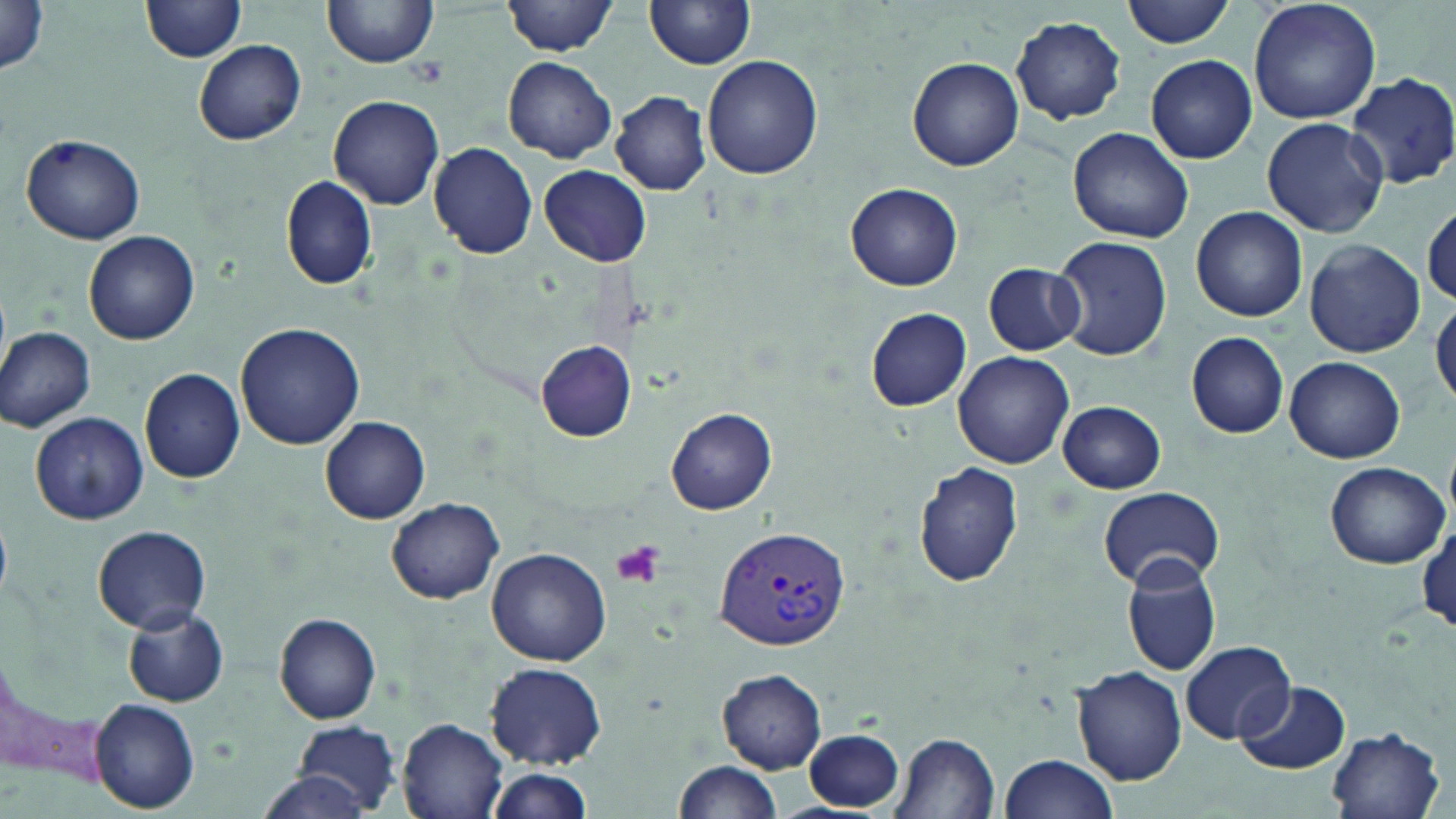
slide_level_diagnosis: Plasmodium vivax
image_size: 1456×819 pixels
platelet_locations: 'approximate bounding boxes as (x1,y1)-(x2,y2) corner pairs in pixels: (412,57)-(448,87), (612,540)-(667,589)'
plasmodium_vivax_infected_red_blood_cell_locations: 'approximate bounding boxes as (x1,y1)-(x2,y2) corner pairs in pixels: (714,524)-(853,649)'
field_of_view: one of a larger specimen
magnification: 1000x
modality: optical microscopy
uninfected_red_blood_cell_locations: 'approximate bounding boxes as (x1,y1)-(x2,y2) corner pairs in pixels: (323,0)-(437,69), (502,0)-(618,56), (646,0)-(755,70), (1122,0)-(1237,47), (1248,0)-(1382,124), (140,2)-(246,64), (0,4)-(52,77), (1011,16)-(1127,124), (193,38)-(306,146), (700,54)-(824,180), (503,55)-(617,163), (1144,55)-(1258,164), (907,57)-(1024,171), (1347,71)-(1456,190), (611,91)-(712,195), (328,95)-(445,210), (1261,118)-(1389,238), (1067,127)-(1193,244), (20,132)-(146,244), (428,143)-(537,259), (538,165)-(651,266), (280,176)-(379,290), (846,182)-(964,291), (1421,197)-(1456,308), (1191,207)-(1307,322), (82,230)-(200,346), (1052,236)-(1172,361), (1303,239)-(1426,357), (983,261)-(1085,355), (1430,295)-(1456,413), (865,307)-(972,412), (235,321)-(366,450), (0,326)-(97,432), (1187,331)-(1290,439), (535,340)-(637,441), (952,351)-(1074,469), (1283,355)-(1405,463), (139,367)-(245,484), (1057,401)-(1166,492), (666,406)-(776,514), (30,411)-(148,525), (321,416)-(430,523), (1324,461)-(1450,569), (913,462)-(1024,588), (1097,486)-(1226,589), (386,497)-(505,603), (1413,518)-(1456,635), (92,525)-(210,634), (486,547)-(611,666), (1121,557)-(1225,678), (122,606)-(228,706), (273,611)-(383,724), (1181,641)-(1293,745), (485,661)-(607,769), (1070,664)-(1188,786), (716,669)-(827,773), (1233,680)-(1348,774), (90,698)-(200,813), (397,718)-(509,819), (295,719)-(404,816), (1324,728)-(1446,819), (805,729)-(904,811), (891,732)-(1001,819), (996,753)-(1120,819), (674,759)-(783,819), (484,767)-(592,818), (256,771)-(380,819)'
preparation: thin blood smear
stain: May-Grünwald-Giemsa